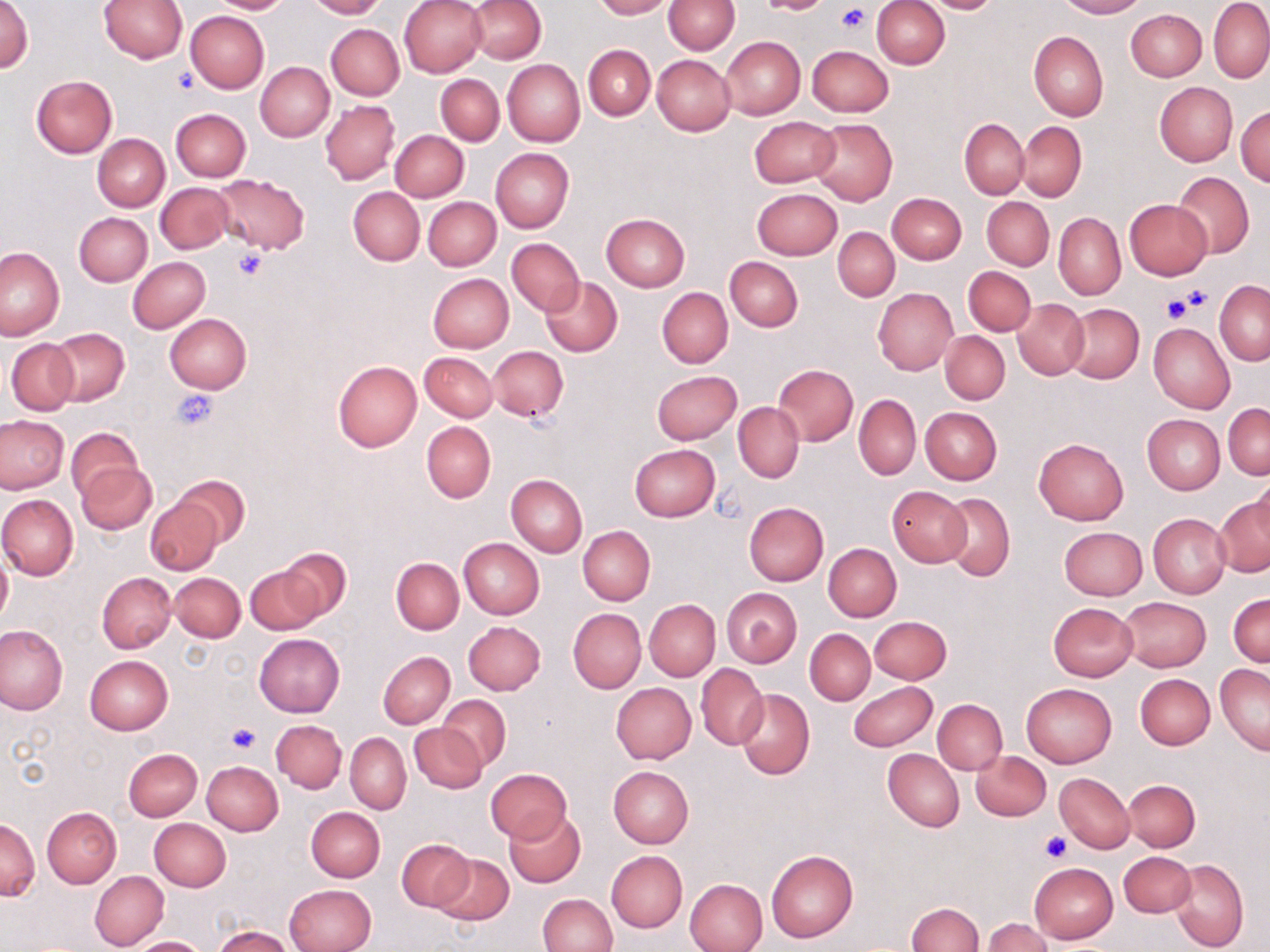
slide_level_diagnosis: negative for blood parasites
image_size: 1270×952 pixels
field_of_view: one of a larger specimen
modality: light microscopy
stain: May-Grünwald-Giemsa
platelet_locations: 'approximate bounding boxes as named x1/y1/x2/y2 corners in pixels: (x1=834, y1=3, x2=872, y2=34), (x1=173, y1=66, x2=200, y2=93), (x1=233, y1=248, x2=268, y2=281), (x1=1177, y1=285, x2=1211, y2=313), (x1=1162, y1=293, x2=1193, y2=323), (x1=172, y1=388, x2=219, y2=430), (x1=225, y1=724, x2=260, y2=755), (x1=1040, y1=830, x2=1072, y2=863)'
uninfected_red_blood_cell_locations: 'approximate bounding boxes as named x1/y1/x2/y2 corners in pixels: (x1=0, y1=0, x2=33, y2=75), (x1=100, y1=0, x2=188, y2=63), (x1=204, y1=0, x2=294, y2=14), (x1=305, y1=0, x2=387, y2=19), (x1=399, y1=0, x2=486, y2=78), (x1=466, y1=0, x2=547, y2=64), (x1=593, y1=0, x2=672, y2=19), (x1=663, y1=0, x2=740, y2=54), (x1=755, y1=0, x2=831, y2=15), (x1=870, y1=0, x2=950, y2=68), (x1=915, y1=0, x2=1004, y2=14), (x1=1056, y1=0, x2=1146, y2=18), (x1=1209, y1=1, x2=1270, y2=82), (x1=1125, y1=9, x2=1206, y2=80), (x1=186, y1=10, x2=268, y2=93), (x1=326, y1=23, x2=404, y2=99), (x1=1029, y1=31, x2=1108, y2=121), (x1=722, y1=37, x2=804, y2=118), (x1=583, y1=45, x2=655, y2=121), (x1=807, y1=45, x2=893, y2=116), (x1=652, y1=54, x2=735, y2=136), (x1=502, y1=58, x2=585, y2=146), (x1=256, y1=61, x2=334, y2=141), (x1=436, y1=73, x2=504, y2=145), (x1=32, y1=75, x2=118, y2=157), (x1=1154, y1=83, x2=1238, y2=166), (x1=320, y1=99, x2=400, y2=185), (x1=1235, y1=105, x2=1270, y2=186), (x1=171, y1=109, x2=250, y2=182), (x1=749, y1=116, x2=839, y2=187), (x1=810, y1=118, x2=898, y2=205), (x1=960, y1=118, x2=1029, y2=199), (x1=1017, y1=121, x2=1087, y2=202), (x1=390, y1=129, x2=469, y2=201), (x1=93, y1=133, x2=170, y2=211), (x1=490, y1=147, x2=574, y2=233), (x1=1170, y1=171, x2=1255, y2=259), (x1=215, y1=175, x2=309, y2=253), (x1=156, y1=182, x2=235, y2=253), (x1=348, y1=186, x2=424, y2=265), (x1=751, y1=188, x2=841, y2=261), (x1=886, y1=192, x2=967, y2=264), (x1=424, y1=196, x2=501, y2=271), (x1=982, y1=197, x2=1053, y2=270), (x1=1124, y1=199, x2=1213, y2=281), (x1=75, y1=212, x2=153, y2=286), (x1=1053, y1=212, x2=1125, y2=300), (x1=601, y1=213, x2=690, y2=291), (x1=833, y1=227, x2=899, y2=301), (x1=505, y1=237, x2=585, y2=315), (x1=0, y1=247, x2=66, y2=340), (x1=128, y1=257, x2=210, y2=332), (x1=725, y1=257, x2=803, y2=331), (x1=963, y1=265, x2=1035, y2=336), (x1=428, y1=273, x2=514, y2=352), (x1=541, y1=277, x2=621, y2=356), (x1=1215, y1=281, x2=1269, y2=364), (x1=657, y1=287, x2=732, y2=368), (x1=873, y1=288, x2=957, y2=376), (x1=1012, y1=298, x2=1089, y2=380), (x1=1064, y1=305, x2=1143, y2=383), (x1=165, y1=313, x2=251, y2=394), (x1=1149, y1=322, x2=1235, y2=415), (x1=49, y1=328, x2=129, y2=406), (x1=940, y1=331, x2=1009, y2=405), (x1=5, y1=338, x2=79, y2=415), (x1=489, y1=346, x2=568, y2=421), (x1=419, y1=352, x2=497, y2=422), (x1=332, y1=361, x2=422, y2=452), (x1=773, y1=364, x2=857, y2=446), (x1=651, y1=370, x2=742, y2=445), (x1=853, y1=395, x2=921, y2=481), (x1=733, y1=403, x2=804, y2=482), (x1=1223, y1=404, x2=1269, y2=480), (x1=921, y1=407, x2=1002, y2=485), (x1=1142, y1=414, x2=1225, y2=494), (x1=0, y1=415, x2=69, y2=493), (x1=421, y1=421, x2=496, y2=502), (x1=66, y1=426, x2=143, y2=501), (x1=1034, y1=437, x2=1129, y2=525), (x1=629, y1=443, x2=721, y2=521), (x1=76, y1=461, x2=157, y2=534), (x1=1252, y1=472, x2=1270, y2=551), (x1=506, y1=473, x2=587, y2=557), (x1=177, y1=475, x2=249, y2=548), (x1=886, y1=486, x2=972, y2=566), (x1=0, y1=494, x2=78, y2=580), (x1=940, y1=494, x2=1015, y2=580), (x1=144, y1=495, x2=224, y2=575), (x1=1214, y1=495, x2=1269, y2=578), (x1=744, y1=502, x2=829, y2=585), (x1=1148, y1=513, x2=1231, y2=598), (x1=578, y1=526, x2=654, y2=605), (x1=1058, y1=526, x2=1149, y2=600), (x1=459, y1=538, x2=544, y2=618), (x1=823, y1=543, x2=901, y2=621), (x1=275, y1=546, x2=352, y2=620), (x1=0, y1=547, x2=12, y2=627), (x1=392, y1=558, x2=463, y2=634), (x1=244, y1=564, x2=324, y2=635), (x1=97, y1=572, x2=176, y2=652), (x1=171, y1=573, x2=245, y2=642), (x1=721, y1=587, x2=802, y2=667), (x1=1228, y1=593, x2=1269, y2=667), (x1=1119, y1=596, x2=1211, y2=671), (x1=645, y1=599, x2=720, y2=681), (x1=1048, y1=602, x2=1137, y2=681), (x1=568, y1=609, x2=646, y2=692), (x1=860, y1=615, x2=944, y2=752), (x1=869, y1=616, x2=951, y2=684), (x1=463, y1=621, x2=546, y2=695), (x1=0, y1=624, x2=67, y2=715), (x1=805, y1=629, x2=875, y2=704), (x1=254, y1=634, x2=345, y2=717), (x1=378, y1=651, x2=454, y2=727), (x1=85, y1=655, x2=173, y2=734), (x1=1215, y1=662, x2=1270, y2=756), (x1=696, y1=663, x2=768, y2=749), (x1=1136, y1=674, x2=1214, y2=749), (x1=848, y1=680, x2=938, y2=752), (x1=611, y1=683, x2=697, y2=764), (x1=1021, y1=683, x2=1116, y2=767), (x1=735, y1=688, x2=814, y2=780), (x1=440, y1=695, x2=511, y2=770), (x1=933, y1=699, x2=1007, y2=774), (x1=271, y1=720, x2=346, y2=792), (x1=409, y1=723, x2=486, y2=794), (x1=346, y1=733, x2=410, y2=813), (x1=122, y1=747, x2=203, y2=820), (x1=883, y1=749, x2=963, y2=831), (x1=972, y1=750, x2=1051, y2=820), (x1=201, y1=760, x2=283, y2=835), (x1=608, y1=765, x2=694, y2=847), (x1=485, y1=768, x2=572, y2=842), (x1=1053, y1=772, x2=1136, y2=853), (x1=1124, y1=779, x2=1200, y2=852), (x1=43, y1=808, x2=121, y2=887), (x1=299, y1=808, x2=380, y2=952), (x1=306, y1=808, x2=384, y2=882), (x1=504, y1=810, x2=585, y2=888), (x1=149, y1=818, x2=231, y2=891), (x1=0, y1=819, x2=39, y2=900), (x1=396, y1=838, x2=473, y2=913), (x1=766, y1=849, x2=859, y2=943), (x1=607, y1=851, x2=686, y2=932), (x1=1119, y1=852, x2=1195, y2=917), (x1=431, y1=854, x2=513, y2=925), (x1=1169, y1=859, x2=1248, y2=951), (x1=1029, y1=863, x2=1117, y2=942), (x1=90, y1=871, x2=169, y2=950), (x1=684, y1=878, x2=767, y2=952), (x1=285, y1=884, x2=376, y2=952), (x1=537, y1=893, x2=617, y2=952), (x1=906, y1=903, x2=983, y2=952), (x1=982, y1=918, x2=1053, y2=952), (x1=213, y1=926, x2=294, y2=951), (x1=131, y1=936, x2=208, y2=952)'
preparation: thin blood film
magnification: 1000x